Name the blood parasite species.
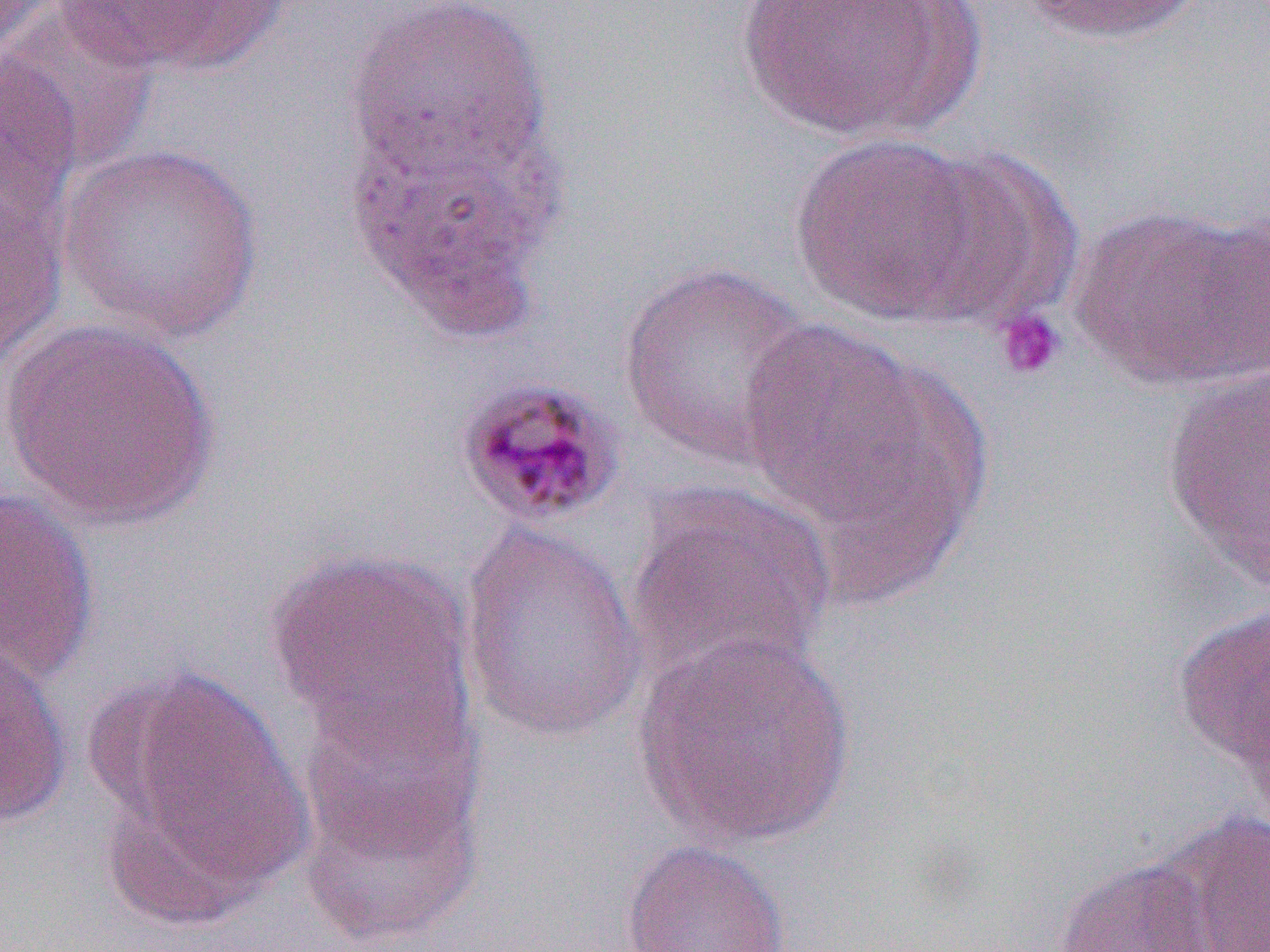
Plasmodium malariae.

Approximate bounding boxes as (x1,y1)-(x2,y2) corner pairs in pixels. Uninfected red blood cell locations: (1013,0)-(1211,46), (2,1)-(159,175), (732,1)-(967,141), (58,2)-(283,77), (342,2)-(552,185), (0,54)-(83,237), (345,96)-(567,338), (788,131)-(993,325), (57,143)-(266,343), (901,145)-(1083,327), (0,182)-(68,372), (1071,203)-(1269,391), (617,260)-(821,472), (735,313)-(967,564), (1,317)-(221,530), (1160,364)-(1270,591), (625,484)-(836,693), (0,486)-(100,686), (458,521)-(649,745), (266,548)-(477,758), (1172,602)-(1270,769), (634,630)-(859,850), (0,637)-(72,829), (108,671)-(311,902), (294,677)-(490,934), (1148,808)-(1270,952), (620,838)-(793,952), (1053,855)-(1220,952). Platelet locations: (994,307)-(1067,380). Plasmodium malariae-infected red blood cell locations: (454,375)-(627,531). Optical microscopy. Single field of view. Image is 1270×952 pixels. Thin blood film. Captured at 1000x magnification.